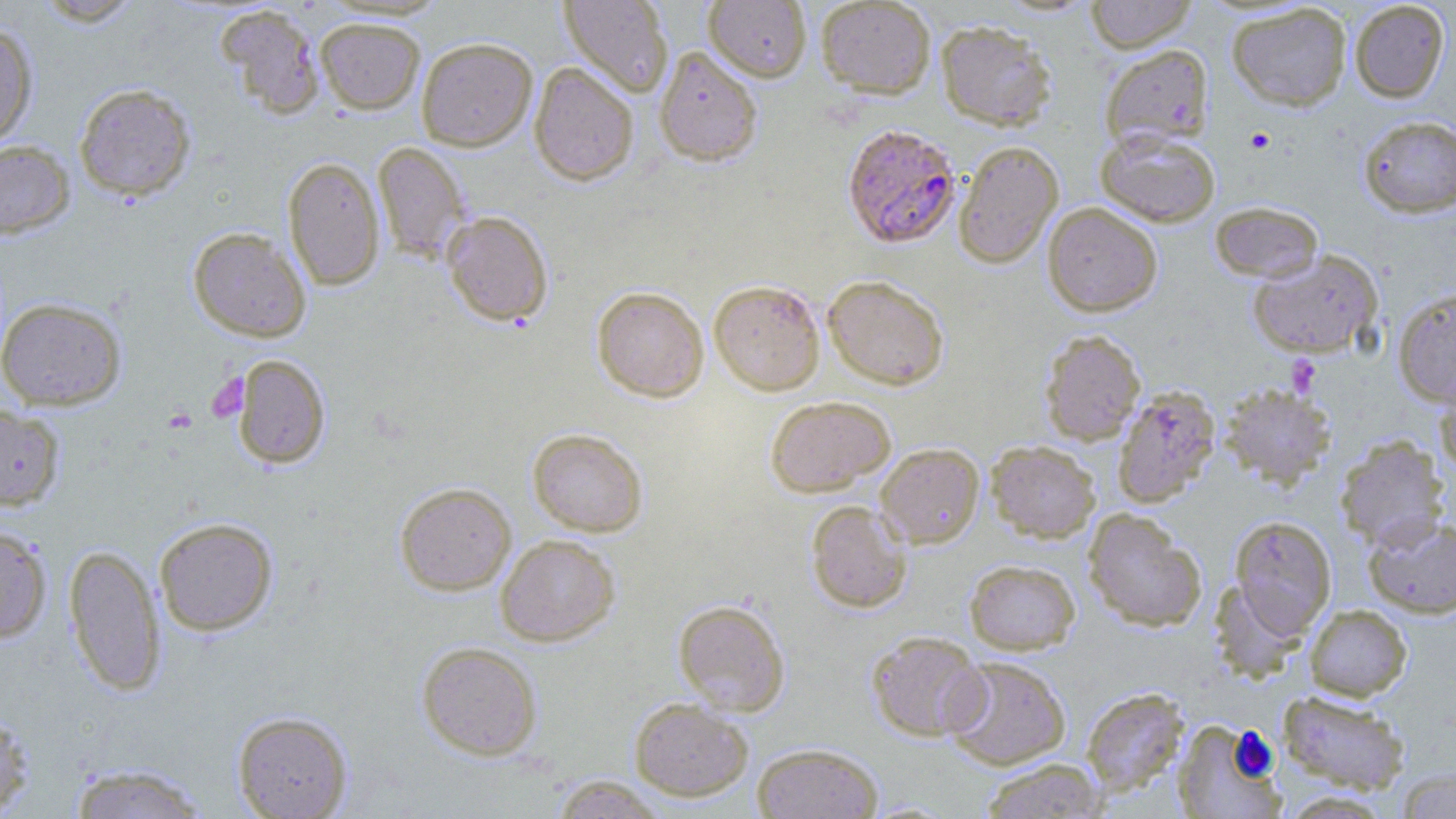
Summary:
  - Coordinate format: approximate bounding boxes as (x1, y1, x2, y2) in pixels
  - Plasmodium falciparum-infected red blood cell locations: (841, 123, 961, 249)
  - Platelet locations: (1245, 127, 1275, 154), (1286, 355, 1322, 396), (207, 372, 249, 422)
  - Uninfected red blood cell locations: (32, 0, 144, 26), (559, 0, 674, 98), (816, 0, 936, 98), (1085, 0, 1198, 52), (703, 1, 812, 82), (1349, 1, 1450, 103), (1227, 3, 1351, 111), (215, 5, 325, 120), (315, 17, 425, 114), (936, 20, 1056, 130), (0, 21, 38, 148), (416, 36, 538, 151), (1099, 43, 1213, 150), (654, 46, 763, 166), (529, 61, 639, 186), (74, 83, 196, 201), (1357, 114, 1456, 218), (1095, 128, 1221, 227), (0, 141, 75, 238), (372, 141, 470, 263), (954, 141, 1064, 269), (282, 157, 385, 291), (1042, 202, 1163, 317), (1210, 202, 1324, 283), (441, 210, 553, 326), (188, 227, 312, 342), (1247, 250, 1383, 359), (822, 274, 949, 391), (709, 279, 826, 395), (591, 286, 709, 402), (1393, 287, 1456, 408), (0, 297, 126, 410), (1039, 330, 1146, 446), (232, 354, 330, 468), (1435, 373, 1456, 482), (1219, 384, 1336, 490), (1111, 387, 1221, 509), (765, 395, 895, 496), (0, 404, 65, 510), (527, 427, 649, 537), (1335, 435, 1450, 551), (986, 440, 1101, 543), (875, 443, 984, 549), (394, 482, 516, 595), (805, 500, 913, 613), (1083, 509, 1207, 632), (1229, 515, 1337, 636), (1363, 515, 1456, 619), (154, 517, 278, 635), (0, 525, 52, 643), (495, 534, 620, 646), (64, 544, 166, 696), (964, 559, 1080, 655), (1209, 579, 1309, 682), (673, 599, 790, 716), (1305, 605, 1412, 701), (867, 631, 987, 742), (417, 641, 542, 760), (943, 656, 1071, 771), (1081, 686, 1189, 797), (1278, 690, 1411, 795), (629, 697, 753, 801), (0, 706, 35, 817), (232, 710, 353, 819), (1172, 720, 1285, 819), (751, 743, 883, 819), (980, 758, 1108, 818), (67, 763, 212, 819), (1394, 768, 1456, 818), (549, 775, 670, 818)
  - Slide-level diagnosis: Plasmodium falciparum
  - Image size: 1456×819 pixels
  - Field of view: single
  - Preparation: thin blood smear
  - Stain: May-Grünwald-Giemsa
  - Magnification: 1000x
  - Modality: light microscopy